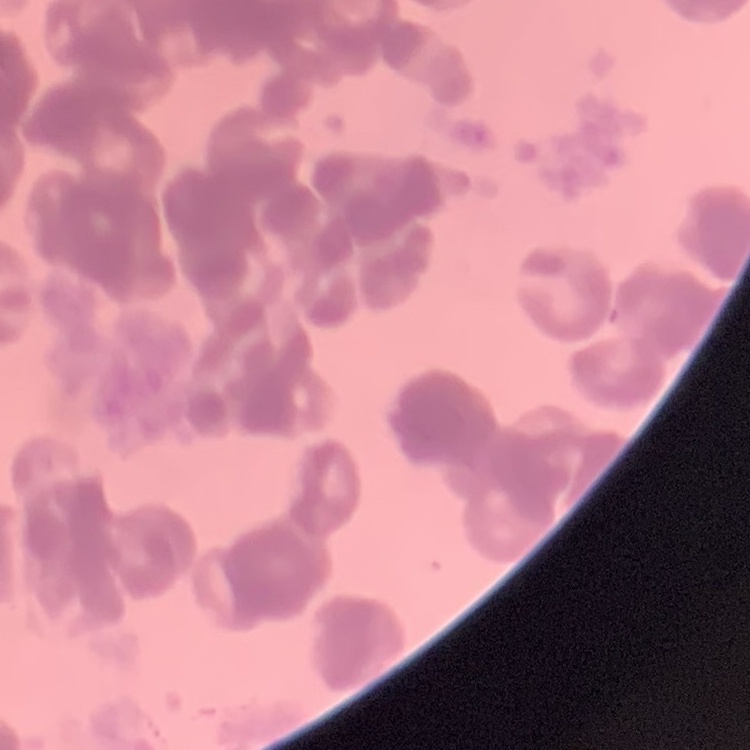
Summary:
  - Erythrocyte morphology: rouleaux formation
  - Image type: square crop of a larger photomicrograph
  - Stain: Field's or Giemsa
  - Preparation: thin blood film